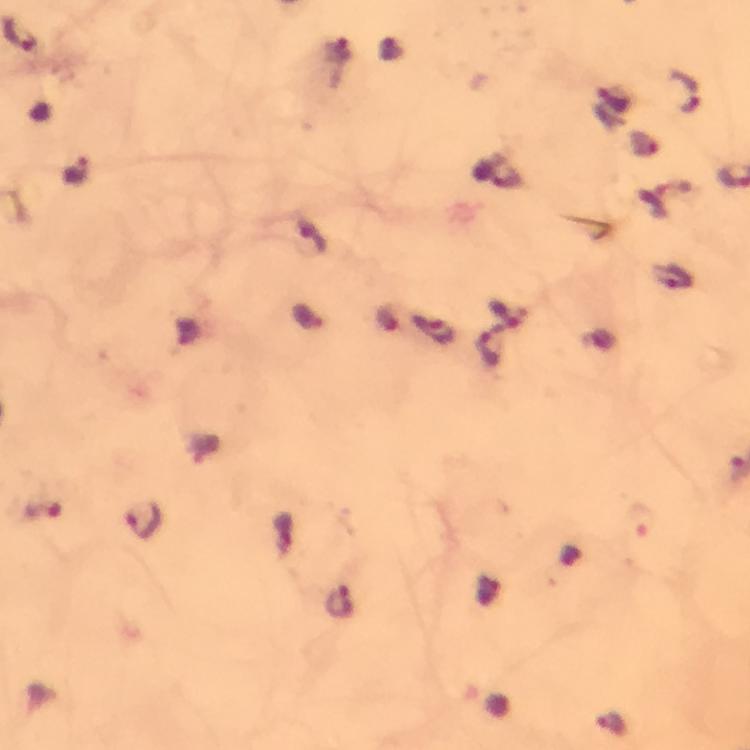
Approximate centers as [x, y] in pixels.
Summary:
  - Malaria parasite locations: [684, 91], [74, 172], [677, 279], [504, 312], [390, 319], [442, 334], [489, 351], [143, 520], [640, 520], [339, 602], [609, 724]
  - Image size: 750×750 pixels
  - Stain: Giemsa
  - Immersion oil: applied
  - Magnification: 100x
  - Preparation: thick blood smear
  - Capture: smartphone mounted on the microscope
  - Cropped from: a single field of view
  - Context: from a diagnostic examination for malaria